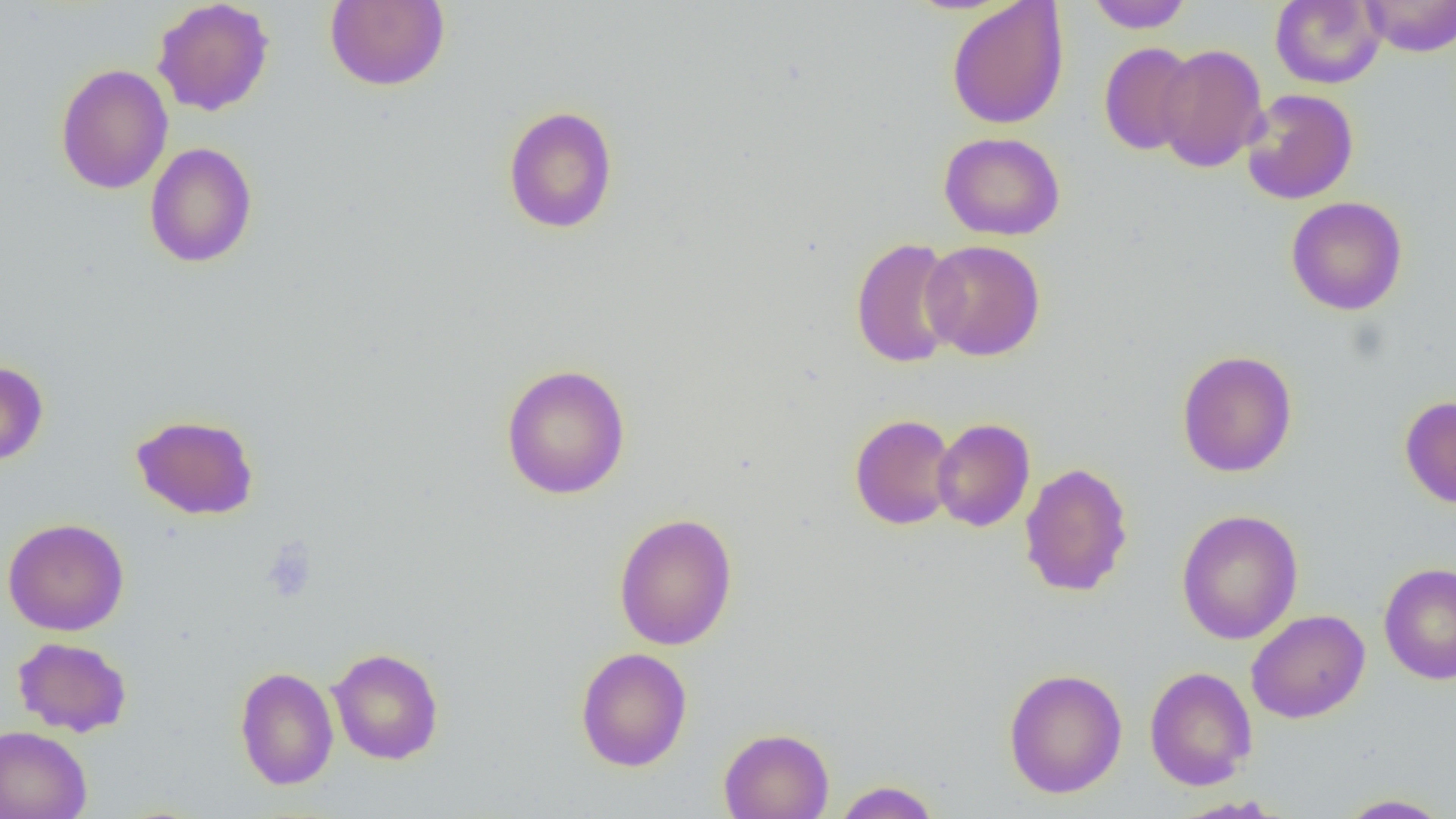

{
  "slide_level_diagnosis": "negative for blood parasites",
  "preparation": "thin blood film",
  "image_size": "1456×819 pixels",
  "platelet_locations": "approximate bounding boxes as (x1,y1)-(x2,y2) corner pairs in pixels: (260,538)-(317,603)",
  "uninfected_red_blood_cell_locations": "approximate bounding boxes as (x1,y1)-(x2,y2) corner pairs in pixels: (151,0)-(275,116), (325,0)-(450,91), (1084,0)-(1194,33), (1270,0)-(1385,88), (1360,0)-(1456,57), (946,1)-(1069,129), (1098,42)-(1199,156), (1154,43)-(1268,172), (55,64)-(174,194), (1241,88)-(1359,205), (502,105)-(619,234), (939,131)-(1066,241), (144,142)-(258,268), (1285,196)-(1408,315), (849,237)-(963,369), (921,239)-(1046,361), (1176,350)-(1298,477), (0,361)-(49,466), (500,363)-(631,500), (1399,395)-(1456,508), (849,413)-(958,530), (130,414)-(260,520), (932,418)-(1035,532), (1019,462)-(1134,597), (1176,508)-(1304,645), (613,512)-(738,651), (2,517)-(130,636), (1378,563)-(1456,685), (1246,609)-(1370,724), (12,637)-(132,737), (575,646)-(692,772), (327,647)-(444,765), (234,665)-(338,791), (1144,666)-(1257,790), (1003,667)-(1127,798), (0,725)-(92,819), (718,727)-(834,819), (833,780)-(942,819), (1334,793)-(1453,818)",
  "modality": "light microscopy",
  "field_of_view": "one of a larger specimen",
  "magnification": "1000x"
}